Assess the morphology of the red blood cells.
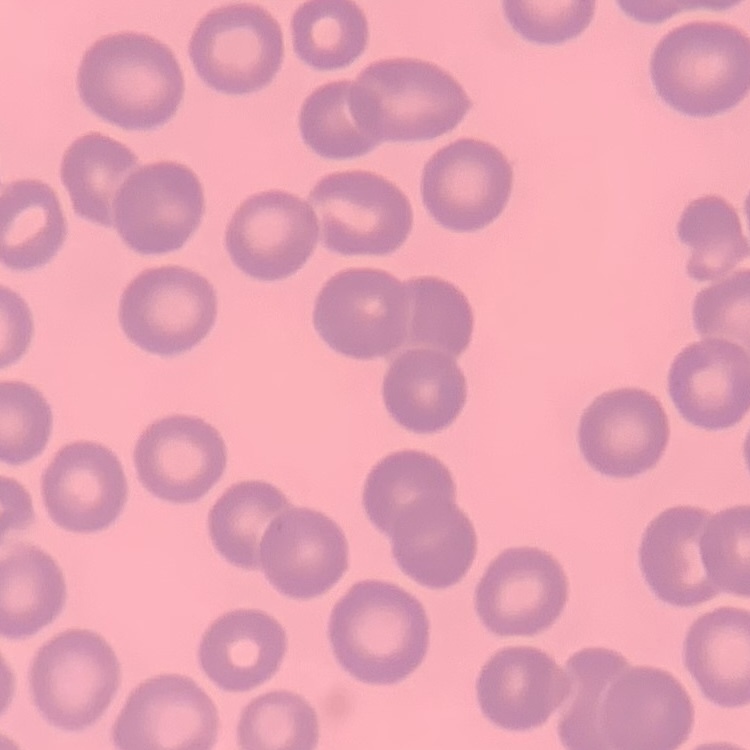
They show no rouleaux formation.

preparation = thin blood smear
image type = square crop of a larger photomicrograph
stain = Field's or Giemsa